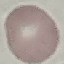
{
  "result": "no malaria parasites detected",
  "preparation": "thin smear",
  "capture": "smartphone camera at the microscope eyepiece",
  "image_type": "automatically extracted cell patch, resized to 64 × 64 pixels",
  "stain": "Giemsa"
}